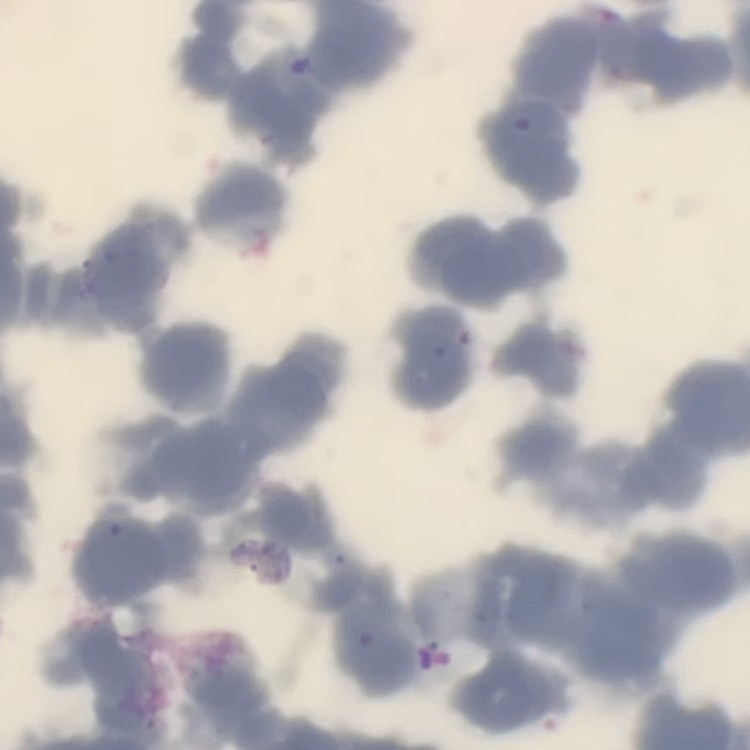

The red blood cells show rouleaux formation. Thin blood film. Stained with either Field's or Giemsa. One tile cut from a larger photomicrograph.